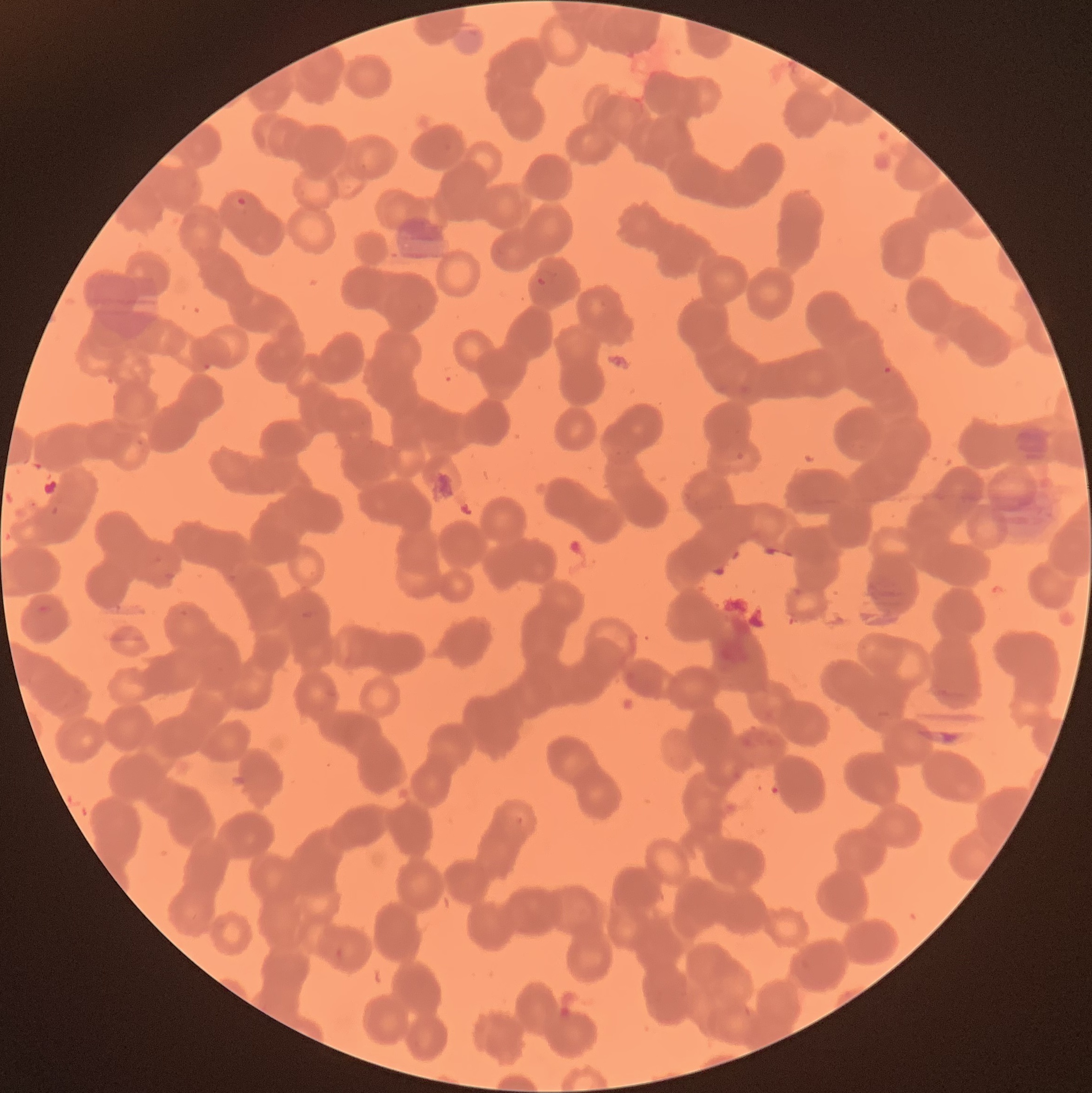
modality: optical microscopy
preparation: thin blood smear
plasmodium_parasite_locations: 'approximate bounding boxes as named x1/y1/x2/y2 corners in pixels: (x1=236, y1=195, x2=248, y2=208), (x1=535, y1=275, x2=548, y2=288), (x1=883, y1=365, x2=892, y2=375)'
image_size: 1092×1093 pixels
red_blood_cell_morphology: rouleaux formation